Assess the morphology of the red blood cells.
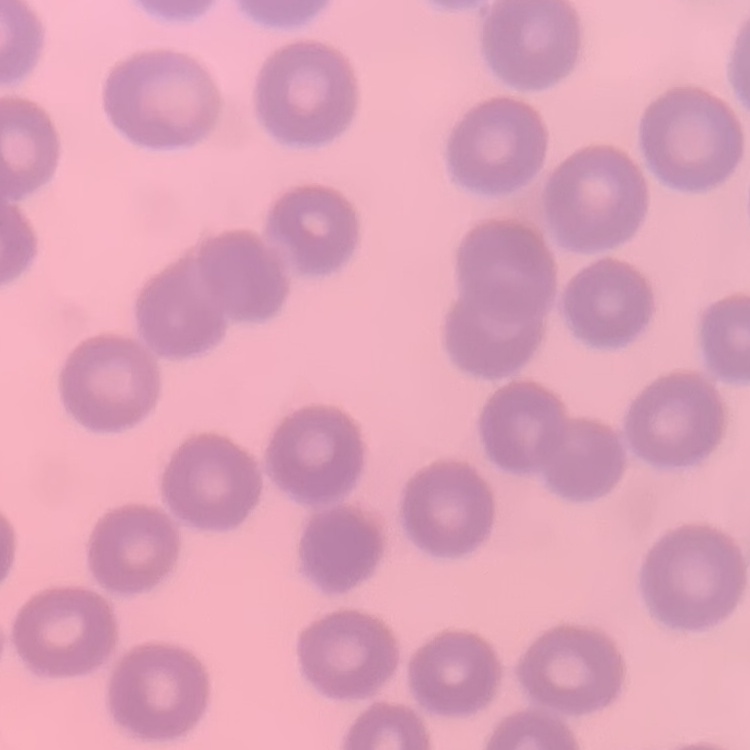

They show no rouleaux formation.

Thin peripheral smear. One tile cut from a larger photomicrograph. Field's or Giemsa stain.